Assess this cell for malaria.
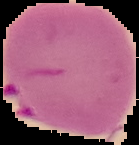

It is parasitized.

image type = segmented cell region on a black background
preparation = thin blood smear
image size = 139×145 pixels